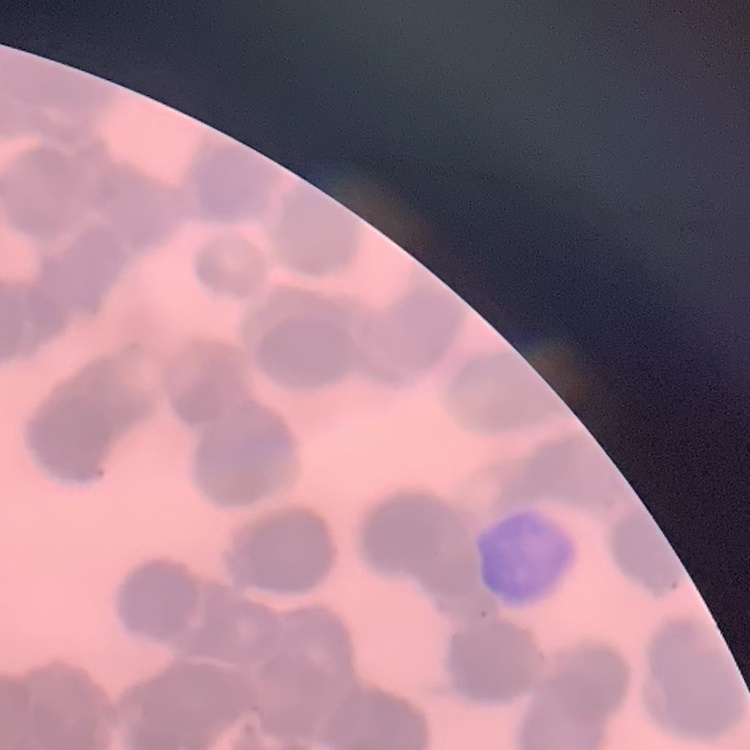

{
  "red_blood_cell_morphology": "rouleaux formation",
  "stain": "Field's or Giemsa",
  "image_type": "square crop of a larger photomicrograph",
  "preparation": "thin blood film"
}